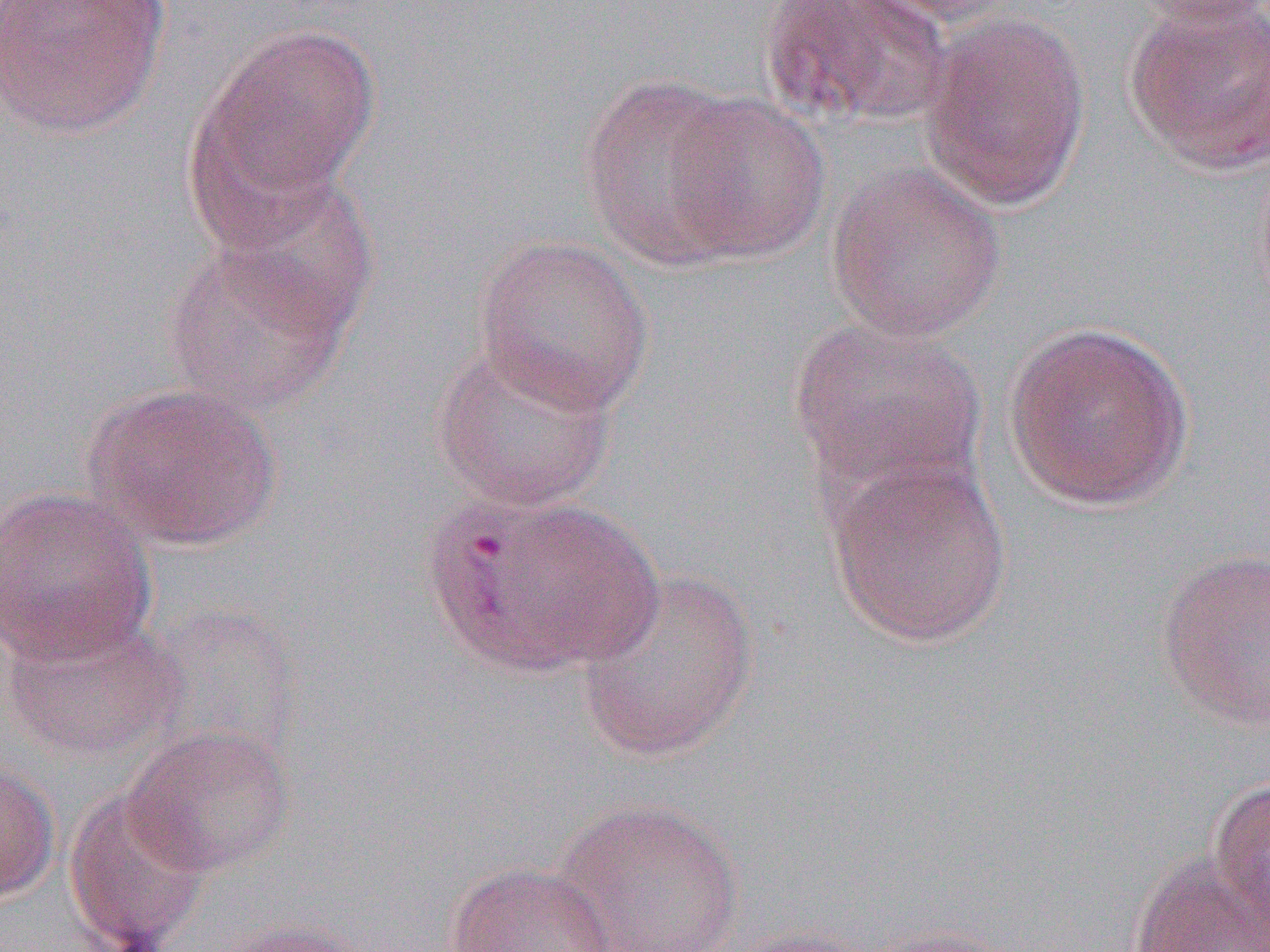

Approximate bounding boxes as (x1, y1, x2, y2) in pixels. Uninfected red blood cell locations: (0, 0, 171, 139), (759, 0, 955, 127), (848, 0, 1026, 28), (1129, 0, 1270, 28), (1122, 1, 1270, 175), (919, 12, 1091, 211), (198, 23, 380, 210), (580, 74, 752, 269), (662, 92, 830, 264), (826, 161, 1006, 343), (212, 174, 381, 342), (473, 235, 655, 415), (160, 239, 353, 419), (788, 318, 988, 495), (1001, 319, 1196, 512), (428, 338, 620, 514), (82, 381, 284, 552), (824, 453, 1014, 649), (0, 486, 158, 665), (431, 494, 659, 675), (1157, 548, 1270, 733), (574, 569, 759, 762), (144, 602, 307, 762), (1, 615, 187, 762), (123, 725, 297, 877), (0, 759, 60, 906), (1207, 778, 1270, 937), (62, 786, 213, 951), (551, 798, 747, 952), (1128, 852, 1270, 952), (444, 862, 617, 952), (214, 919, 379, 952), (850, 923, 1030, 952), (721, 925, 888, 952). Slide-level diagnosis: Plasmodium vivax. Captured at 1000x magnification. Single field of view. Thin blood film. Image is 1270×952 pixels. Light microscopy.